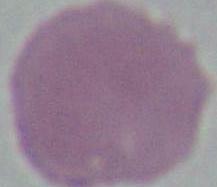
modality = photomicrograph
identification = red blood cell
magnification = 1000x